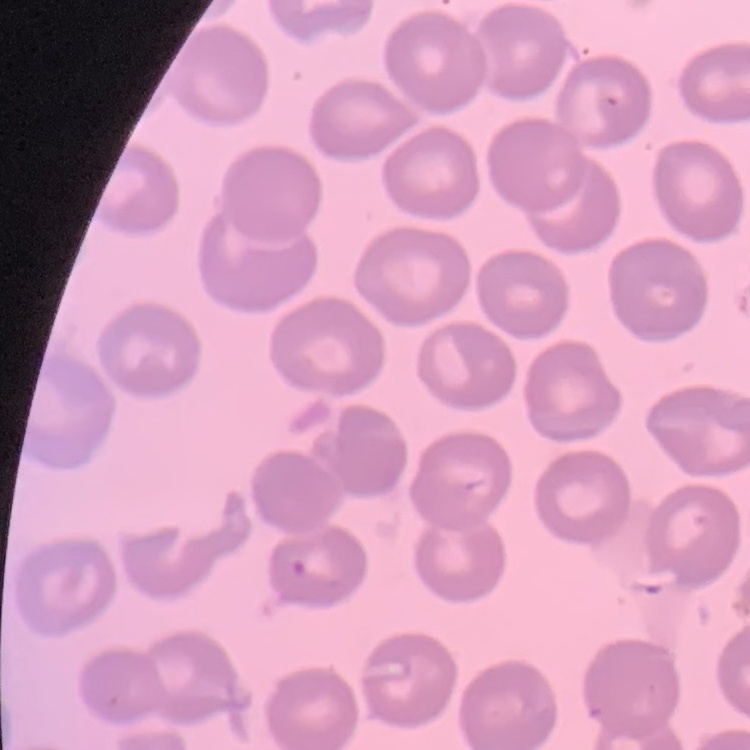
red_blood_cell_morphology: no rouleaux formation
image_type: one tile cut from a larger photomicrograph
preparation: thin blood smear
stain: Field's or Giemsa